Give the position of every malaria parasite and every leukocyte.
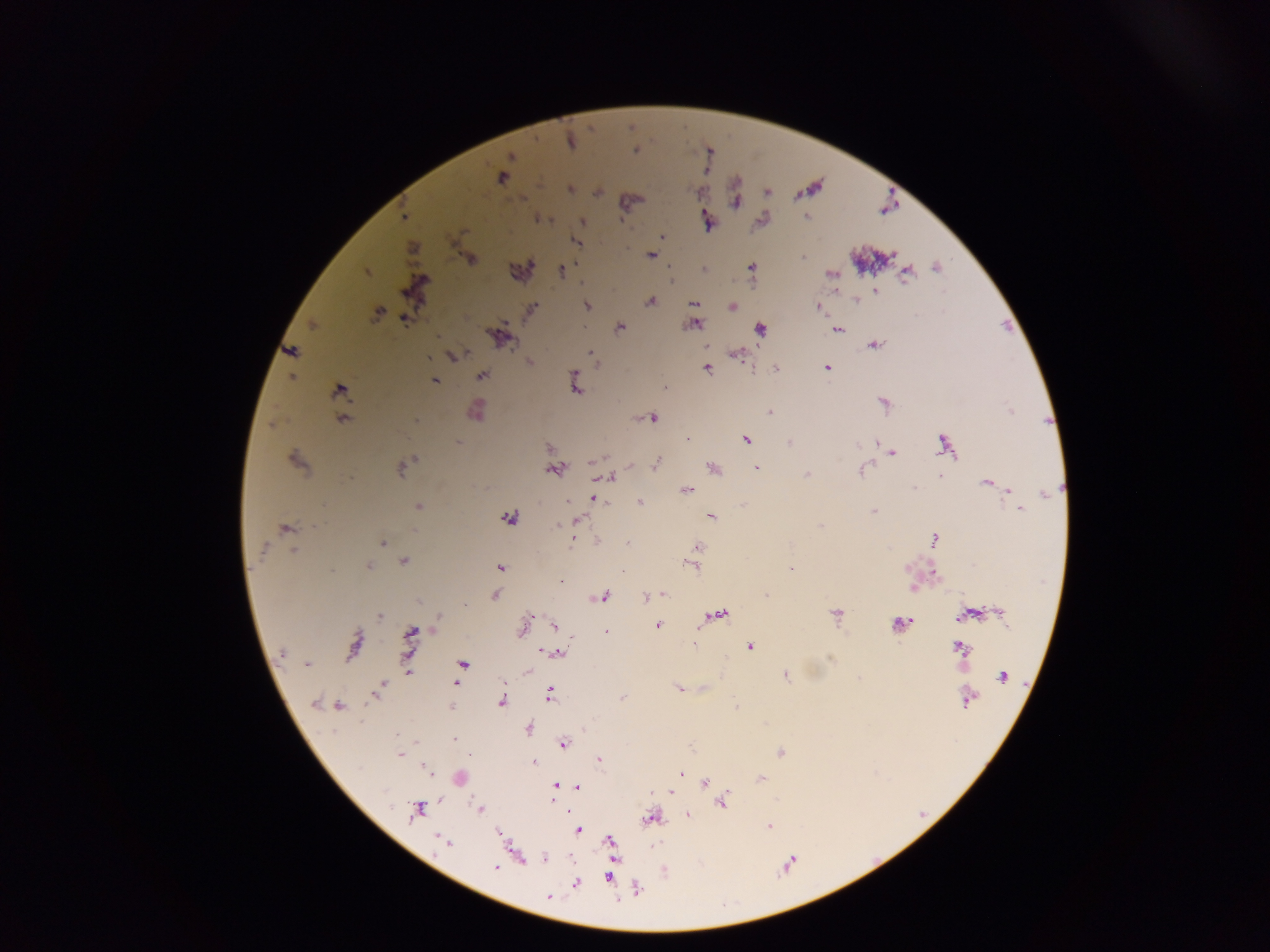

Approximate centers as (x, y) in pixels.
Malaria parasites: (570, 140), (635, 151), (511, 156), (501, 178), (570, 189), (404, 217), (583, 222), (463, 231), (662, 237), (575, 241), (412, 248), (651, 255), (803, 256), (471, 259), (752, 267), (562, 270), (366, 272), (831, 274), (906, 274), (875, 291), (856, 300), (650, 302), (694, 303), (587, 305), (818, 306), (732, 307), (532, 309), (378, 313), (404, 320), (312, 324), (695, 325), (620, 327), (759, 330), (838, 330), (499, 337), (874, 345), (291, 351), (591, 353), (738, 354), (455, 356), (429, 357), (529, 362), (827, 367), (776, 368), (707, 369), (482, 375), (574, 375), (292, 377), (434, 381), (575, 384), (665, 387), (339, 389), (342, 410), (476, 411), (770, 413), (653, 418), (343, 419), (415, 420), (746, 439), (458, 443), (789, 443), (876, 443), (944, 443), (550, 447), (892, 452), (415, 459), (296, 461), (592, 462), (656, 464), (630, 465), (714, 468), (756, 468), (401, 470), (554, 470), (862, 470), (807, 474), (940, 476), (611, 478), (986, 483), (914, 488), (686, 490), (1008, 490), (1047, 493), (593, 498), (567, 502), (640, 502), (418, 507), (1019, 509), (873, 511), (711, 516), (510, 517), (579, 519), (558, 525), (820, 525), (285, 529), (415, 530), (934, 539), (573, 540), (383, 542), (627, 543), (698, 547), (263, 549), (293, 550), (403, 562), (368, 566), (692, 566), (500, 568), (790, 569), (934, 574), (561, 582), (913, 588), (495, 594), (604, 595), (664, 595), (766, 595), (646, 597), (835, 613), (721, 614), (1000, 614), (963, 615), (380, 617), (438, 621), (903, 623), (554, 626), (657, 626), (523, 627), (410, 632), (606, 632), (694, 644), (353, 645), (749, 646), (959, 648), (283, 652), (557, 653), (408, 662), (463, 664), (307, 665), (409, 670), (527, 672), (785, 676), (1002, 676), (456, 683), (383, 684), (678, 688), (380, 690), (376, 694), (550, 695), (621, 698), (967, 701), (501, 702), (314, 703), (337, 706), (528, 730), (397, 735), (454, 739), (563, 744), (780, 752), (399, 754), (469, 755), (600, 759), (534, 763), (428, 770), (681, 773), (761, 779), (705, 782), (556, 786), (578, 786), (670, 792), (721, 802), (479, 809), (418, 811), (687, 814), (650, 818), (769, 826), (577, 830), (499, 833), (610, 841), (446, 843), (545, 858), (494, 867), (609, 877), (576, 883), (548, 897).
No leukocytes observed.

Summary:
  - Country: Ghana
  - Capture: mobile-phone photograph through a microscope
  - Image size: 1270×952 pixels
  - Preparation: thick blood smear
  - Field of view: single